State the preparation type.
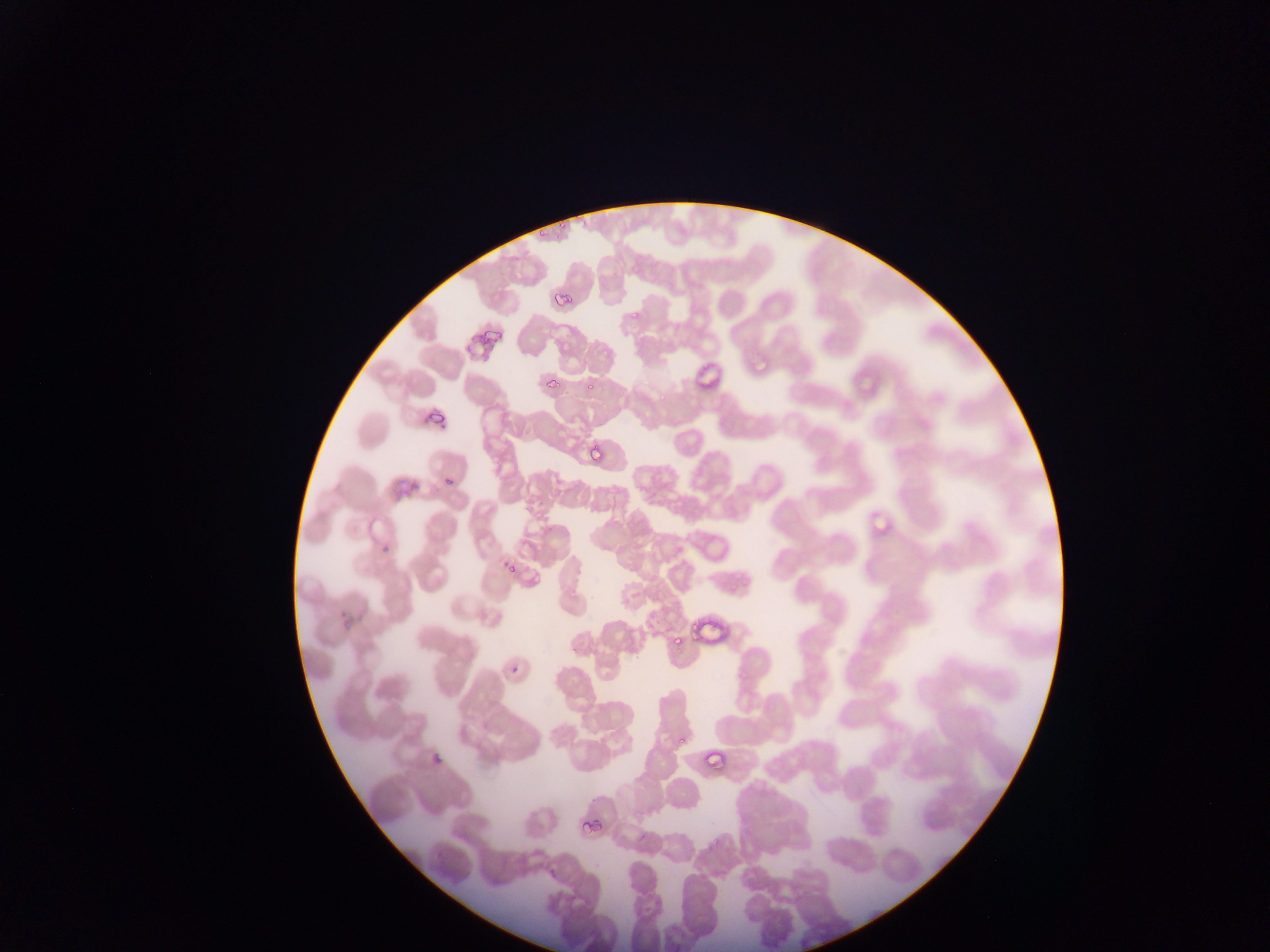

This is a thin smear.

plasmodium_parasite_locations: 'approximate bounding boxes as left top right bottom in pixels: 558 219 569 231; 534 226 548 242; 552 287 576 312; 630 309 641 322; 486 325 504 346; 755 360 769 372; 694 361 721 386; 541 375 563 387; 586 378 596 392; 429 410 447 424; 589 448 603 463; 440 472 458 484; 873 516 889 536; 383 545 397 557; 504 561 516 575; 688 615 702 641; 672 631 686 647; 510 662 522 675; 676 734 686 748; 700 745 730 776; 425 749 443 768; 587 810 608 836'
image_size: 1270×952 pixels
capture: mobile-phone photograph through a microscope
country: Ghana
field_of_view: single